Report the malaria status of this cell.
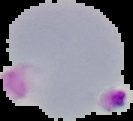
It is parasitized.

{
  "image_size": "133×121 pixels",
  "image_type": "segmented cell region on a black background",
  "preparation": "thin blood smear"
}